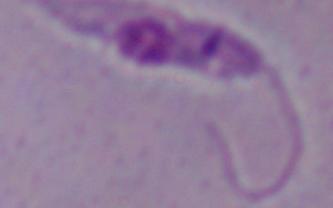

Summary:
  - Identification: Leishmania
  - Modality: photomicrograph
  - Magnification: 1000x